Identify the parasite.
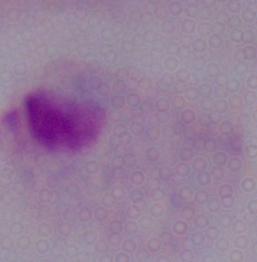
A trichomonad.

Photomicrograph. 1000x magnification.